Comment on the morphology of the erythrocytes.
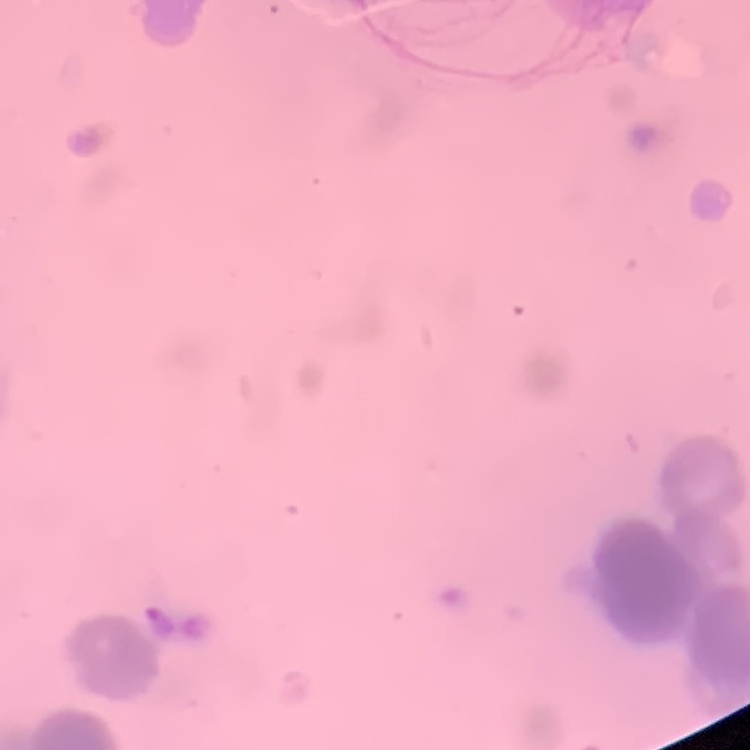
Rouleaux formation.

{
  "image_type": "one tile cut from a larger photomicrograph",
  "stain": "Field's or Giemsa",
  "preparation": "thin peripheral smear"
}